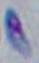

identification = Toxoplasma gondii
modality = photomicrograph
magnification = 1000x